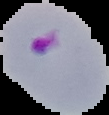
Summary:
  - Image type: segmented cell region on a black background
  - Preparation: thin blood film
  - Image size: 109×115 pixels
  - Result: malaria parasites identified